Outline each Plasmodium vivax-infected red blood cell.
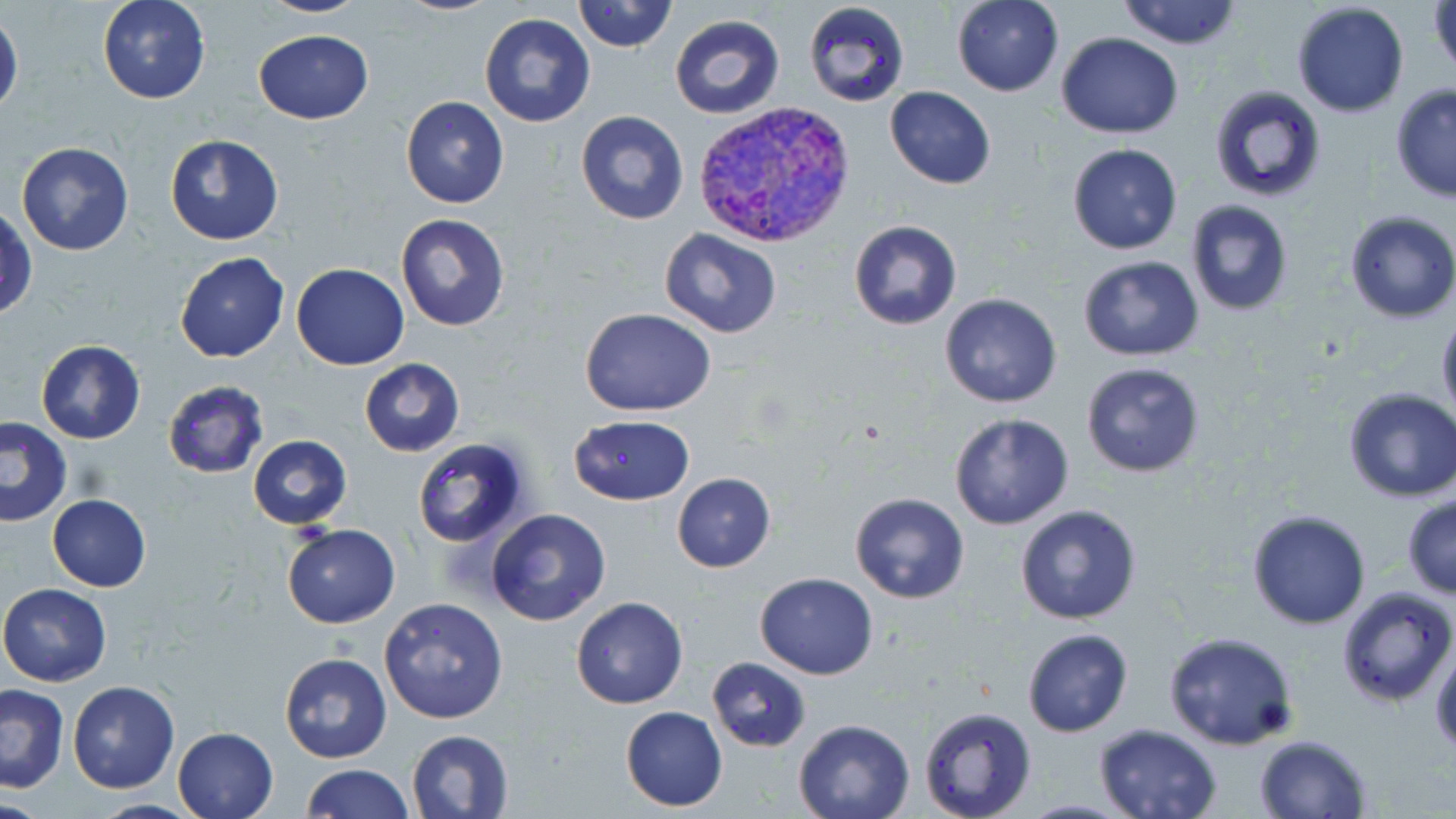
Approximate bounding boxes as (x1, y1, x2, y2) in pixels.
Plasmodium vivax-infected red blood cells: (690, 100, 856, 250).

Summary:
  - Uninfected red blood cell locations: (96, 0, 211, 104), (255, 0, 370, 18), (393, 0, 504, 15), (572, 0, 677, 53), (951, 0, 1063, 97), (1116, 0, 1243, 50), (1428, 0, 1455, 81), (804, 1, 909, 108), (1292, 2, 1409, 118), (0, 11, 22, 116), (480, 12, 597, 127), (670, 13, 784, 120), (253, 29, 376, 124), (1058, 33, 1183, 139), (1208, 85, 1327, 204), (1389, 85, 1456, 202), (884, 86, 997, 188), (401, 97, 509, 208), (576, 109, 687, 224), (165, 134, 283, 244), (17, 141, 134, 256), (1067, 143, 1182, 255), (1186, 200, 1294, 316), (0, 203, 37, 322), (1345, 210, 1456, 323), (395, 214, 510, 331), (848, 220, 962, 331), (659, 229, 783, 339), (174, 250, 289, 363), (1078, 255, 1203, 360), (291, 263, 409, 370), (939, 293, 1063, 408), (579, 308, 716, 416), (1436, 313, 1456, 421), (36, 340, 145, 443), (359, 359, 464, 456), (1082, 361, 1204, 477), (161, 380, 270, 479), (1342, 387, 1456, 502), (949, 413, 1075, 531), (0, 416, 72, 526), (568, 417, 695, 504), (247, 435, 351, 529), (411, 438, 532, 550), (672, 473, 776, 572), (47, 493, 152, 593), (849, 493, 969, 604), (1401, 493, 1456, 598), (1015, 505, 1143, 625), (485, 509, 612, 627), (1245, 509, 1371, 629), (282, 523, 400, 628), (755, 573, 878, 679), (0, 582, 111, 685), (1335, 585, 1454, 705), (378, 596, 509, 723), (571, 596, 688, 708), (1022, 628, 1132, 737), (1161, 632, 1300, 751), (1430, 634, 1456, 757), (278, 650, 392, 764), (705, 657, 813, 752), (67, 680, 179, 793), (0, 684, 69, 793), (621, 705, 727, 812), (918, 706, 1038, 819), (792, 718, 916, 819), (1094, 724, 1222, 818), (171, 726, 279, 819), (405, 730, 513, 818), (1253, 734, 1373, 819), (302, 764, 413, 819), (83, 799, 204, 818)
  - Slide-level diagnosis: Plasmodium vivax
  - Preparation: thin blood smear
  - Stain: May-Grünwald-Giemsa
  - Magnification: 1000x
  - Image size: 1456×819 pixels
  - Modality: optical microscopy
  - Field of view: single